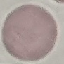

Result: no malaria parasites detected. Cell patch, automatically extracted from a larger field of view and resized to 64 × 64 pixels. Giemsa stain. Acquired by smartphone through the microscope eyepiece. Thin blood film.